Assess the morphology of the erythrocytes.
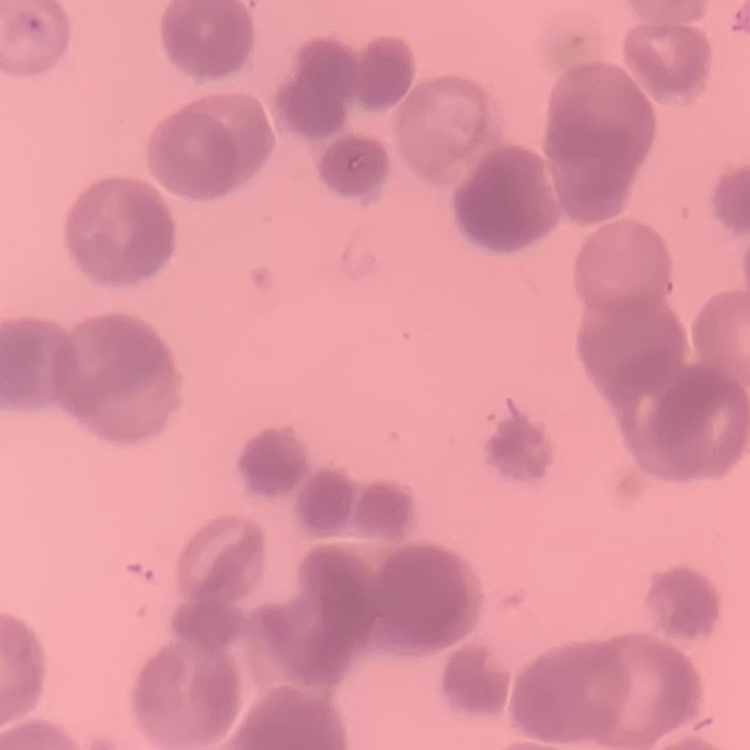
They show rouleaux formation.

Summary:
  - Image type: one tile cut from a larger photomicrograph
  - Preparation: thin blood smear
  - Stain: Field's or Giemsa